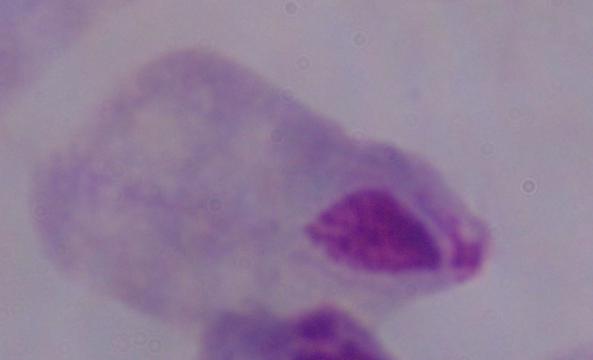

{
  "identification": "trichomonad",
  "magnification": "1000x",
  "modality": "photomicrograph"
}